Point out leukocytes.
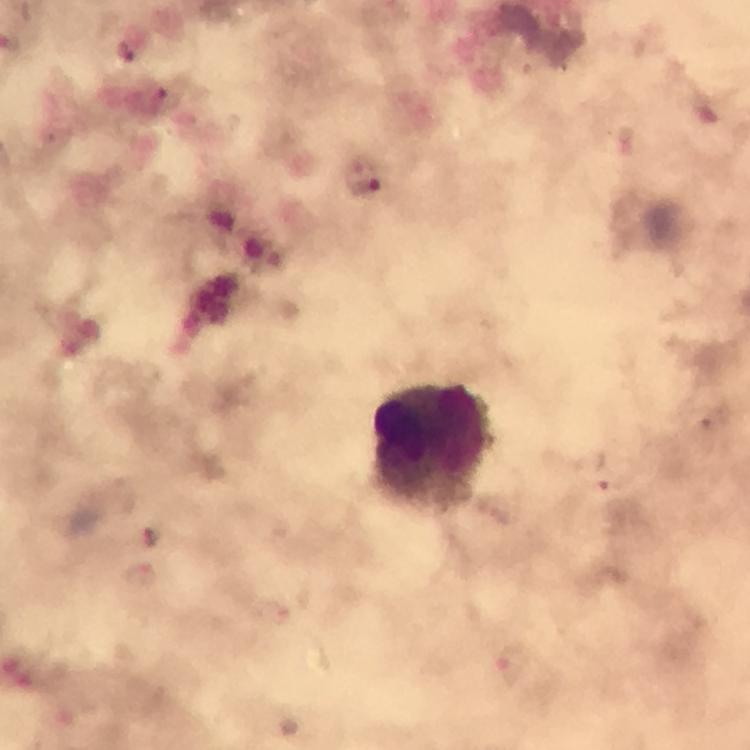

Approximate centers as {x, y} in pixels.
Leukocytes: {432, 446}.

image size = 750×750 pixels
magnification = 100x
context = from a malaria diagnostic workup
capture = smartphone photograph through a microscope
cropped from = a single field of view
preparation = thick blood smear
immersion oil = applied
stain = Giemsa
Plasmodium parasite locations = approximate centers as {x, y} in pixels: {126, 52}, {365, 180}, {604, 477}